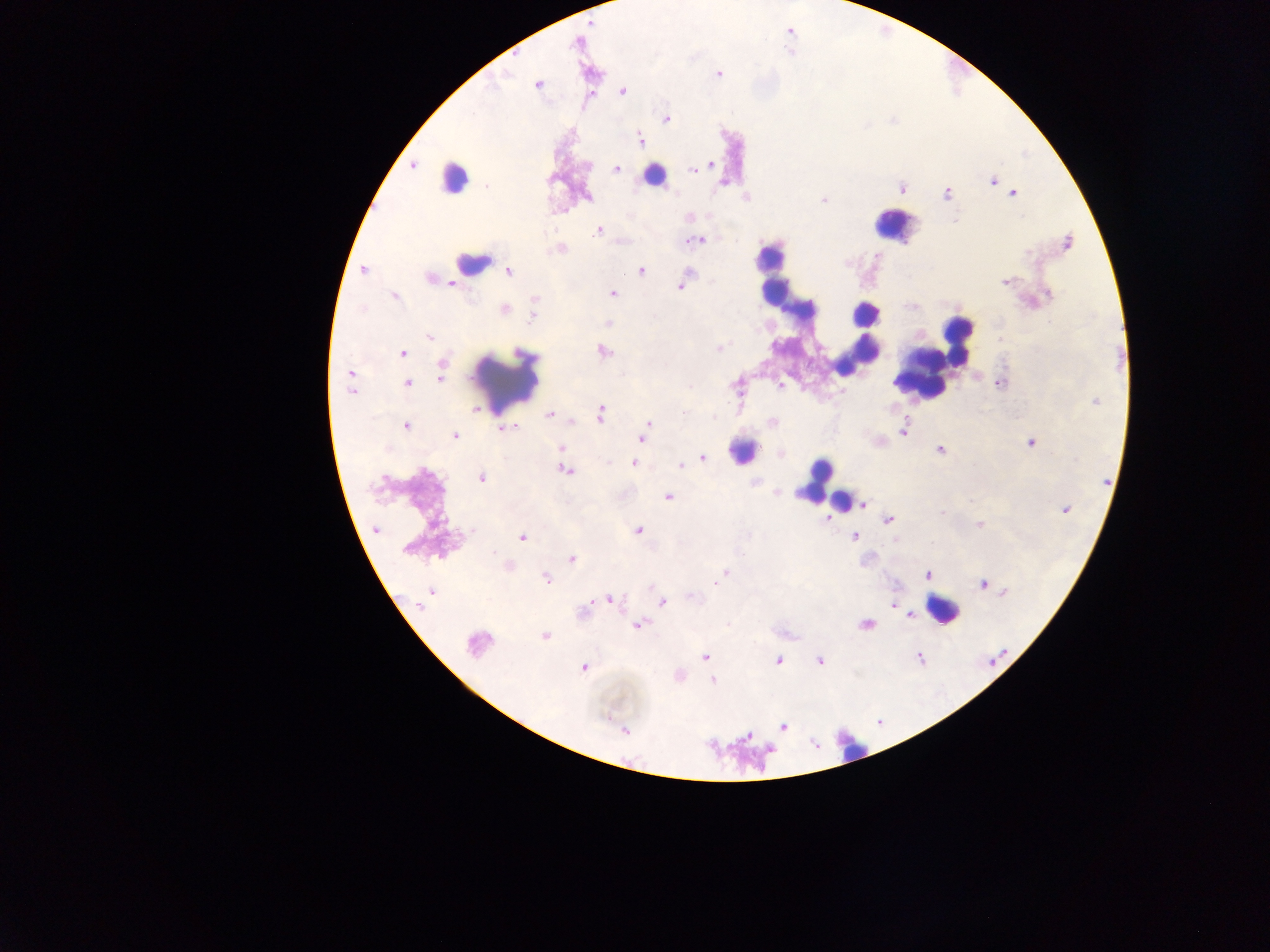

Approximate centers as {x, y} in pixels.
Summary:
  - Malaria parasite locations: {719, 74}, {537, 85}, {622, 92}, {666, 118}, {640, 138}, {711, 164}, {413, 166}, {700, 167}, {617, 169}, {693, 169}, {993, 181}, {723, 183}, {487, 187}, {947, 193}, {1013, 193}, {588, 197}, {823, 199}, {599, 230}, {697, 240}, {1067, 242}, {559, 249}, {362, 271}, {508, 271}, {641, 271}, {1005, 283}, {680, 286}, {612, 293}, {394, 296}, {535, 300}, {504, 310}, {533, 316}, {607, 323}, {429, 336}, {718, 349}, {604, 351}, {403, 354}, {442, 365}, {350, 373}, {440, 378}, {408, 383}, {1000, 383}, {780, 386}, {351, 391}, {1095, 401}, {476, 410}, {549, 414}, {601, 414}, {684, 414}, {772, 422}, {571, 423}, {649, 423}, {406, 426}, {646, 428}, {505, 429}, {903, 430}, {454, 436}, {641, 438}, {1030, 443}, {561, 447}, {940, 450}, {781, 452}, {703, 458}, {634, 463}, {680, 466}, {565, 470}, {481, 478}, {668, 497}, {863, 504}, {1065, 509}, {942, 512}, {828, 519}, {889, 520}, {979, 525}, {638, 530}, {522, 537}, {854, 537}, {572, 558}, {724, 573}, {927, 575}, {545, 579}, {718, 580}, {983, 584}, {1005, 592}, {430, 593}, {693, 596}, {611, 599}, {662, 602}, {421, 603}, {893, 604}, {909, 616}, {728, 624}, {638, 625}, {866, 625}, {544, 636}, {476, 644}, {704, 657}, {918, 658}, {778, 660}, {820, 660}, {584, 667}, {712, 681}, {783, 727}, {625, 730}, {747, 736}
  - Leukocyte locations: {654, 175}, {452, 179}, {892, 224}, {468, 263}, {772, 274}, {806, 308}, {865, 311}, {958, 338}, {859, 354}, {921, 375}, {506, 381}, {742, 453}, {822, 483}, {840, 499}, {946, 609}, {851, 752}
  - Field of view: single
  - Preparation: thick blood film
  - Capture: mobile-phone photograph through a microscope
  - Image size: 1270×952 pixels
  - Country: Ghana